Give the position of every Plasmodium parasite.
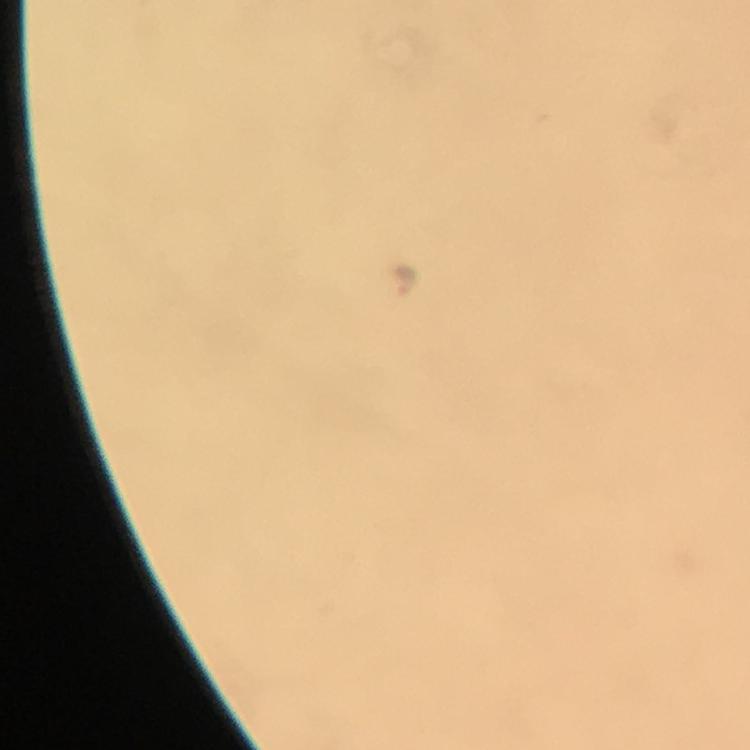
Approximate centers as (x, y) in pixels.
Plasmodium parasites: (406, 279).

{
  "image_size": "750×750 pixels",
  "preparation": "thick blood film",
  "immersion_oil": "applied",
  "context": "from a malaria diagnostic workup",
  "stain": "Giemsa",
  "magnification": "100x",
  "cropped_from": "a single field of view",
  "capture": "smartphone camera through the microscope"
}